Locate every leukocyte (white blood cell).
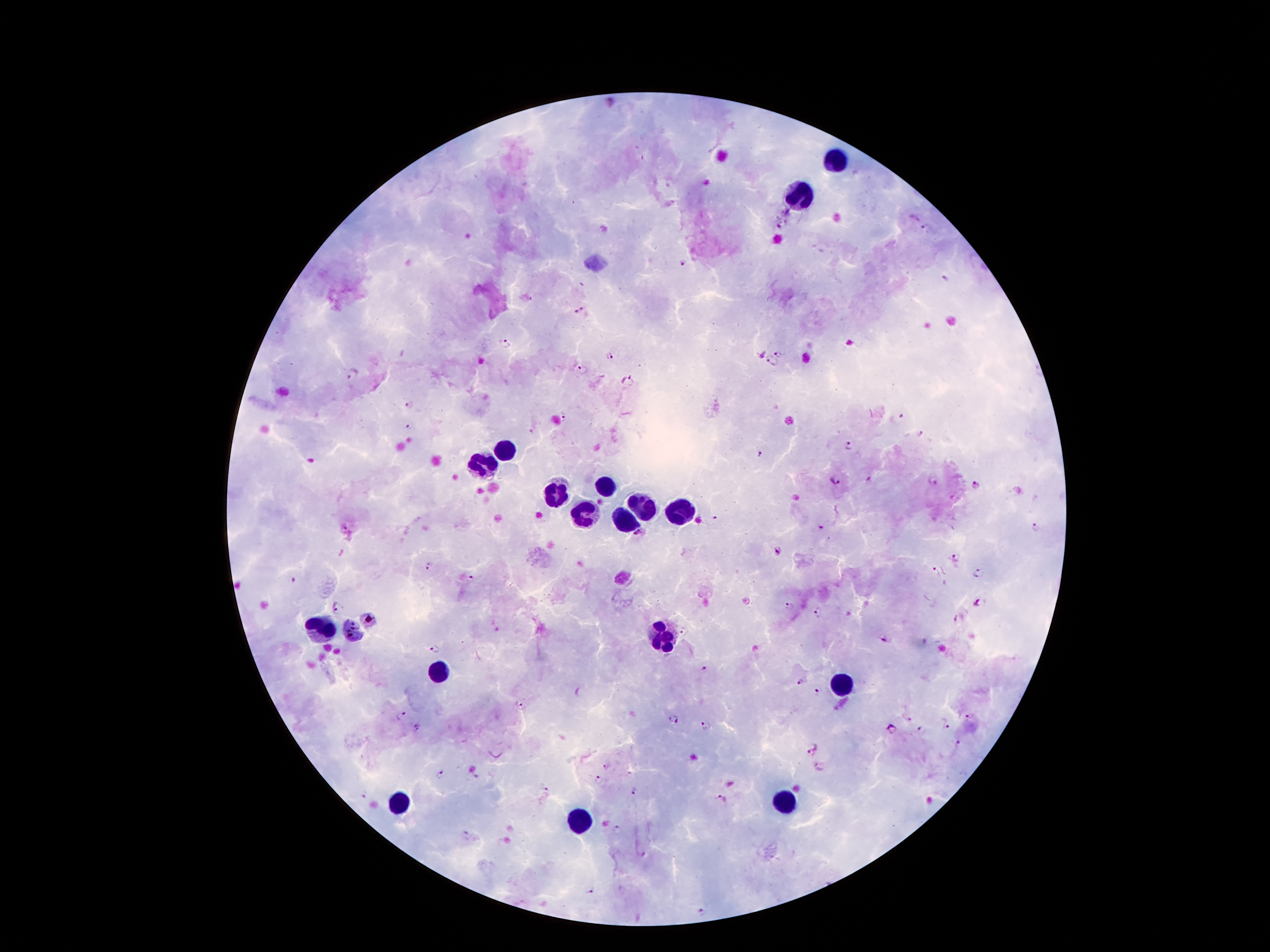

Approximate centers as {x, y} in pixels.
Leukocytes: {839, 160}, {799, 198}, {503, 448}, {484, 467}, {601, 490}, {553, 498}, {641, 509}, {681, 509}, {582, 515}, {624, 521}, {320, 630}, {351, 630}, {660, 636}, {439, 671}, {842, 687}, {396, 796}, {787, 801}, {580, 825}.

malaria parasite locations = {780, 226}, {929, 229}, {682, 263}, {944, 280}, {582, 312}, {504, 342}, {780, 352}, {760, 353}, {609, 356}, {771, 363}, {582, 371}, {353, 373}, {629, 382}, {411, 407}, {566, 416}, {901, 416}, {411, 426}, {920, 432}, {850, 446}, {761, 454}, {833, 479}, {869, 480}, {932, 482}, {974, 486}, {717, 519}, {1035, 527}, {822, 528}, {640, 535}, {780, 552}, {955, 558}, {429, 565}, {936, 571}, {978, 572}, {470, 578}, {294, 579}, {981, 601}, {787, 603}, {339, 608}, {818, 612}, {955, 618}, {368, 621}, {683, 631}, {884, 638}, {435, 648}, {705, 671}, {799, 681}, {818, 691}, {521, 705}, {968, 714}, {401, 715}, {908, 715}, {674, 719}, {947, 724}, {705, 726}, {892, 726}, {417, 727}, {921, 731}, {958, 742}, {811, 745}, {605, 765}, {819, 767}, {438, 774}, {598, 778}, {543, 786}, {636, 791}, {364, 795}, {721, 798}, {618, 830}, {589, 890}, {701, 912}
preparation = thick peripheral-blood smear
capture = smartphone through the microscope eyepiece
patient malaria status = positive for Plasmodium falciparum
image size = 1270×952 pixels
stain = Giemsa
field of view = one from this slide
magnification = 100x